Outline each blood parasite and name the species.
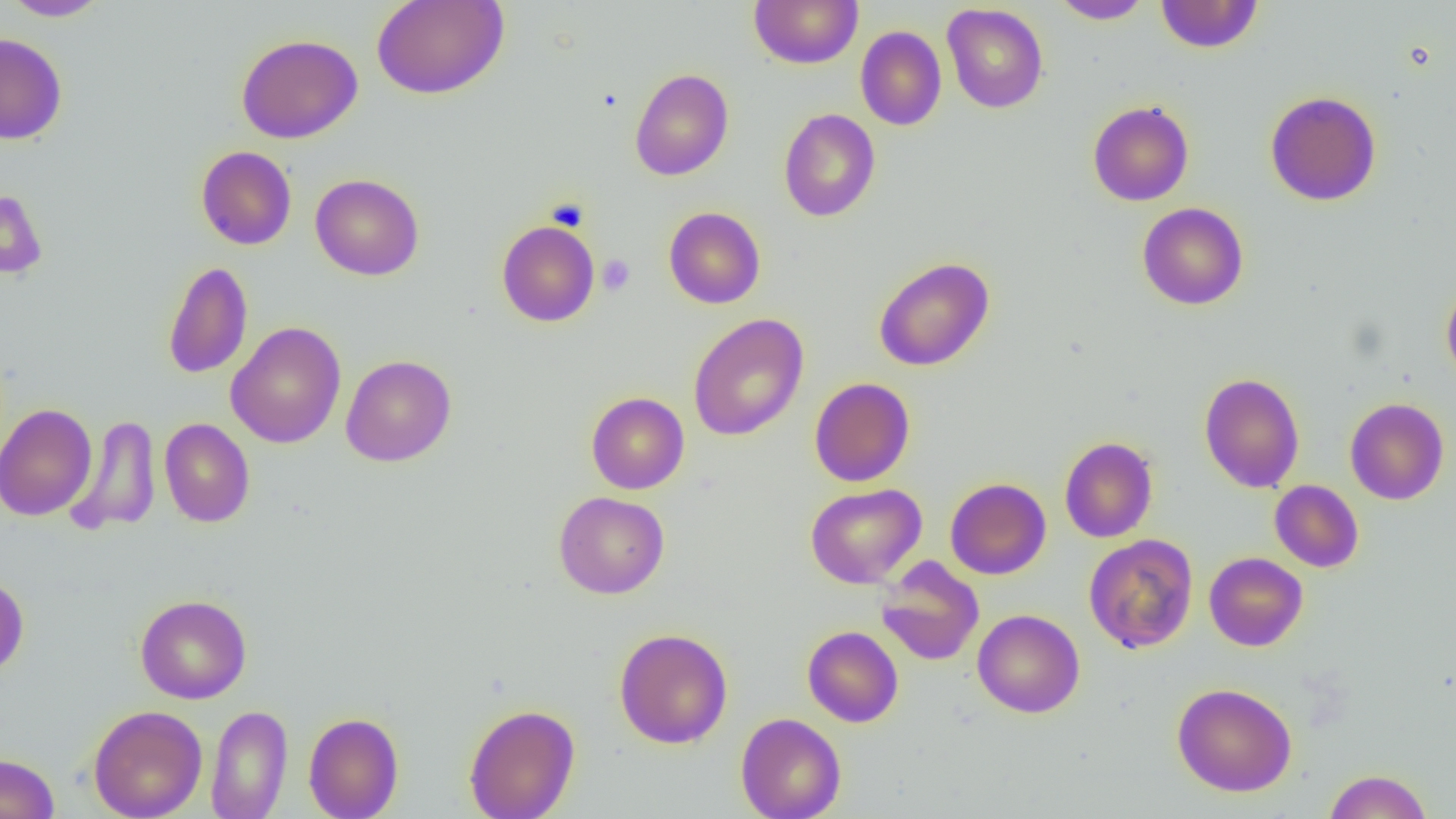

No blood parasites seen.

Approximate bounding boxes as (x1, y1, x2, y2) in pixels. Platelet locations: (597, 254, 635, 295). Uninfected red blood cell locations: (2, 0, 111, 21), (371, 0, 509, 100), (749, 0, 863, 68), (1050, 0, 1154, 24), (1155, 0, 1264, 54), (942, 3, 1048, 113), (855, 26, 946, 130), (0, 33, 68, 145), (235, 33, 363, 144), (630, 67, 734, 180), (1264, 90, 1382, 206), (1087, 100, 1194, 206), (778, 108, 881, 222), (196, 146, 297, 250), (310, 174, 424, 281), (0, 187, 48, 280), (1137, 202, 1249, 310), (663, 206, 765, 309), (496, 220, 600, 327), (872, 256, 995, 372), (162, 260, 253, 380), (1441, 282, 1456, 384), (688, 314, 809, 441), (225, 322, 346, 448), (341, 354, 456, 467), (1199, 372, 1304, 493), (809, 377, 915, 487), (586, 392, 689, 494), (1345, 398, 1449, 505), (0, 404, 98, 521), (65, 414, 161, 535), (159, 418, 255, 528), (1059, 436, 1158, 543), (945, 477, 1051, 580), (1269, 480, 1364, 572), (805, 483, 926, 588), (554, 491, 669, 599), (1083, 534, 1198, 653), (1204, 552, 1308, 651), (877, 558, 985, 666), (0, 573, 29, 677), (135, 594, 252, 704), (972, 609, 1085, 718), (803, 625, 903, 728), (613, 627, 733, 749), (1172, 682, 1297, 797), (464, 703, 580, 819), (206, 704, 293, 819), (88, 705, 207, 819), (303, 711, 404, 819), (735, 713, 847, 819), (0, 753, 59, 819), (1323, 769, 1433, 818). Slide-level diagnosis: no evidence of blood parasites. Captured at 1000x magnification. Optical microscopy. Single field of view. Thin blood smear. Image is 1456×819 pixels.